Report the malaria status of this cell.
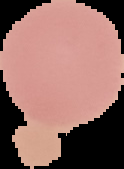

It is uninfected.

Summary:
  - Preparation: thin blood film
  - Image type: segmented cell region with the area outside set to black
  - Image size: 124×169 pixels